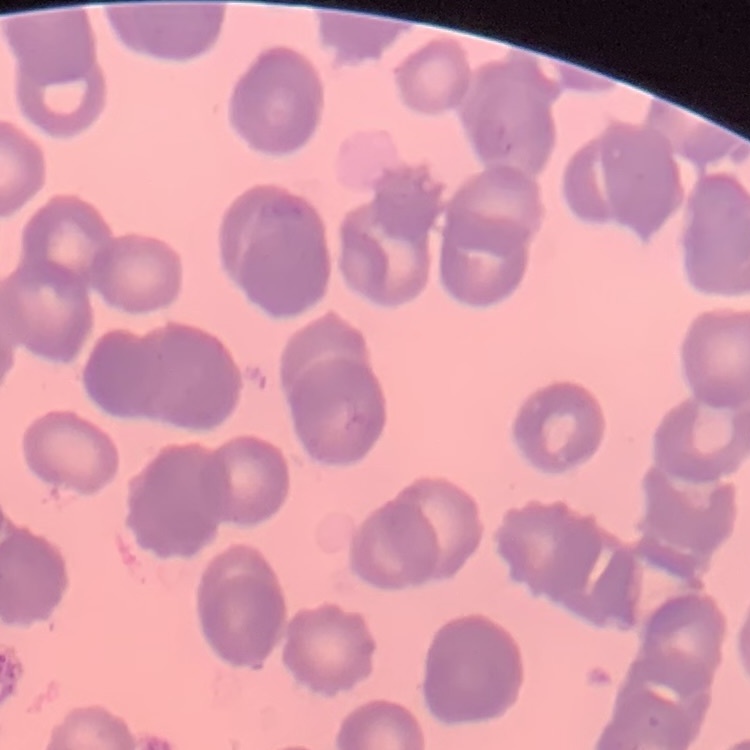
red blood cell morphology = rouleaux formation
stain = Field's or Giemsa
image type = one tile cut from a larger photomicrograph
preparation = thin peripheral smear